Assess this cell for malaria.
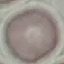

It is uninfected.

{
  "preparation": "thin blood smear",
  "image_type": "automatically extracted cell patch, resized to 64 × 64 pixels",
  "stain": "Giemsa",
  "capture": "smartphone through the microscope eyepiece"
}